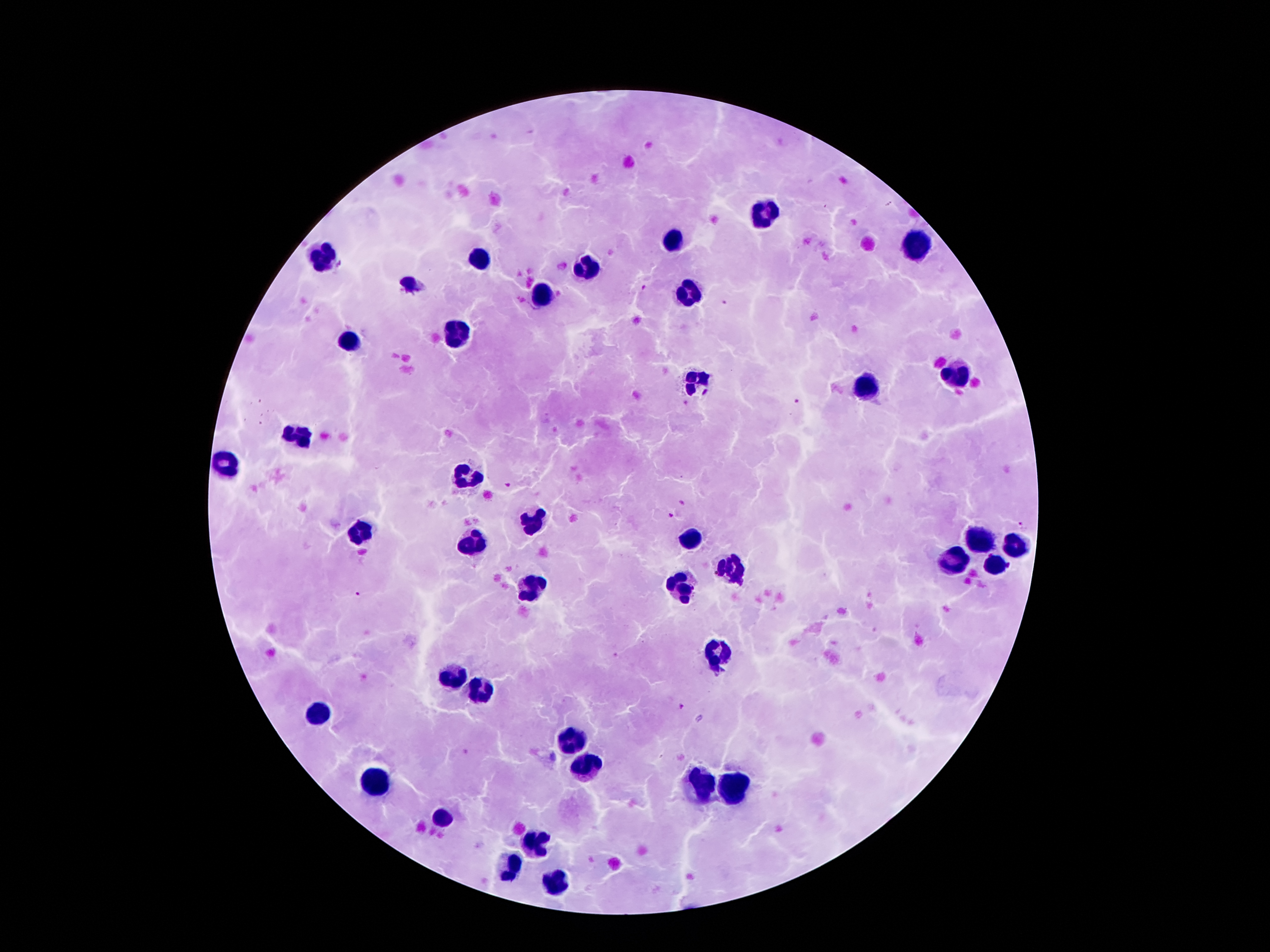
Approximate centers as (x, y) in pixels. Leukocyte locations: (764, 212), (671, 240), (918, 246), (325, 253), (477, 260), (586, 264), (407, 282), (687, 292), (543, 296), (457, 333), (350, 342), (961, 373), (698, 382), (864, 387), (300, 432), (230, 467), (464, 478), (532, 520), (362, 532), (982, 538), (686, 540), (473, 545), (1018, 550), (954, 555), (997, 567), (729, 569), (682, 588), (536, 589), (718, 654), (455, 673), (484, 688), (321, 712), (575, 744), (589, 767), (375, 781), (696, 782), (734, 785), (439, 818), (537, 844), (509, 865), (553, 885). Plasmodium parasite locations: (643, 287), (725, 305), (794, 401), (509, 486), (671, 515), (1024, 525), (359, 594), (681, 706). Single field of view. Giemsa stain. Image is 1270×952 pixels. Patient malaria status: positive for Plasmodium falciparum. Smartphone photograph taken through the microscope eyepiece. Thick blood film. 100x magnification.